Locate every Plasmodium parasite.
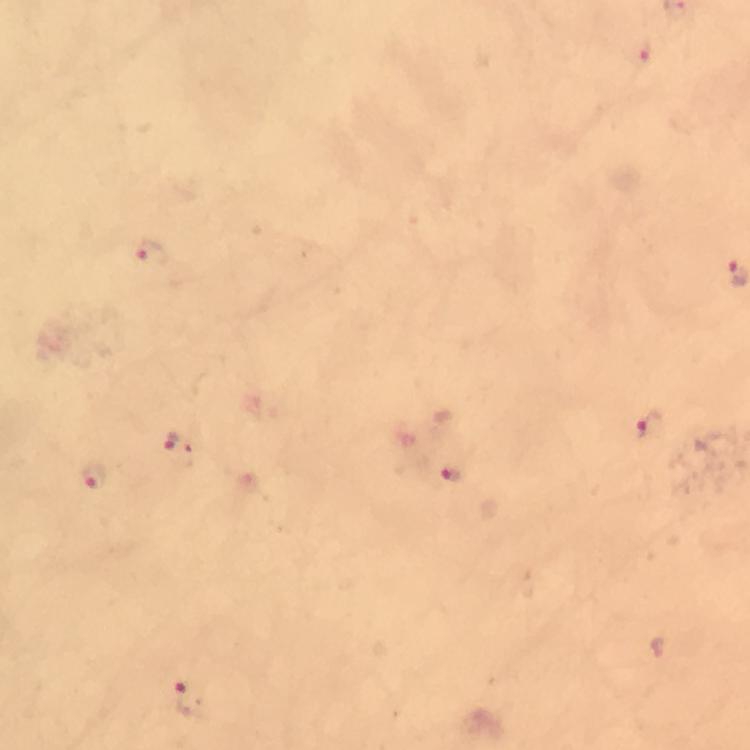
Approximate object centers, in pixels from the top-left corner.
Plasmodium parasites: (x=643, y=59), (x=152, y=255), (x=649, y=430), (x=178, y=447), (x=92, y=476), (x=454, y=479), (x=190, y=701).

immersion oil = applied
preparation = thick blood film
cropped from = a single field of view
stain = Giemsa
image size = 750×750 pixels
context = from a malaria diagnostic workup
capture = smartphone mounted on the microscope
magnification = 100x